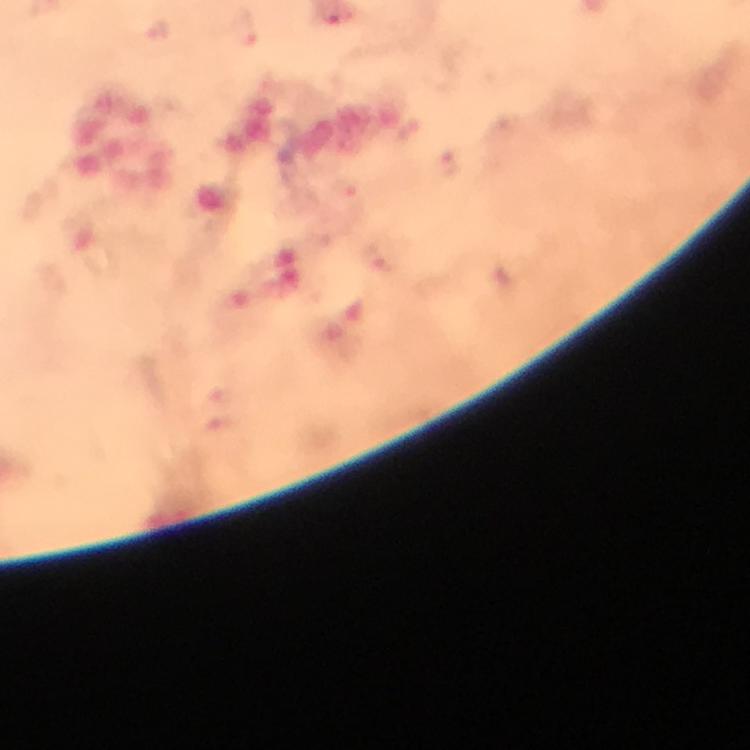

Approximate object centers, in pixels from the top-left corner.
Summary:
  - Malaria parasite locations: (x=346, y=191), (x=377, y=261)
  - Cropped from: a single field of view
  - Preparation: thick blood film
  - Image size: 750×750 pixels
  - Magnification: 100x
  - Context: from a malaria diagnostic workup
  - Immersion oil: applied
  - Stain: Giemsa
  - Capture: smartphone camera through the microscope